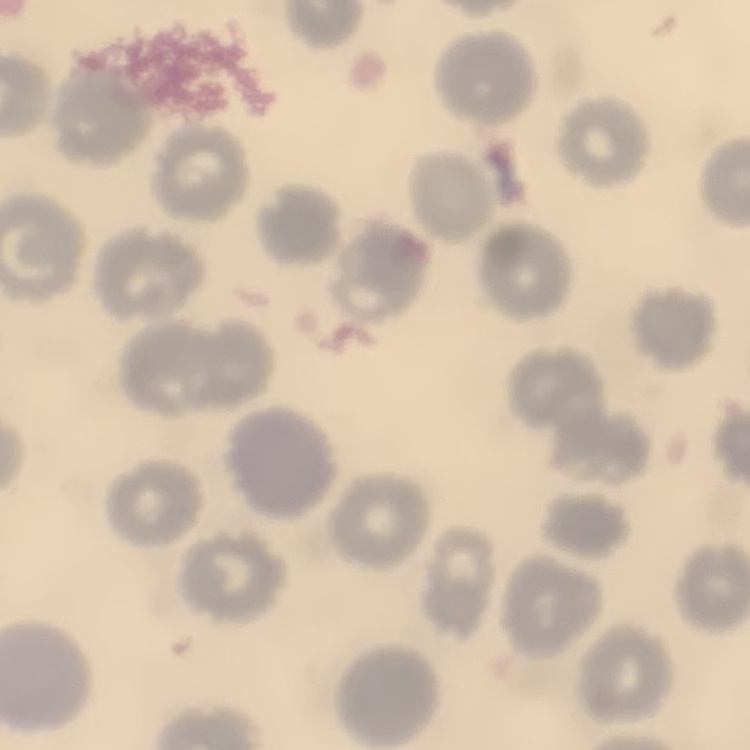
Summary:
  - Erythrocyte morphology: no rouleaux formation
  - Preparation: thin peripheral smear
  - Stain: Field's or Giemsa
  - Image type: square crop of a larger photomicrograph